State which parasite is depicted.
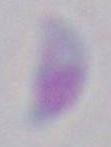

Toxoplasma gondii.

Micrograph. Captured at 1000x magnification.